Assess for malaria.
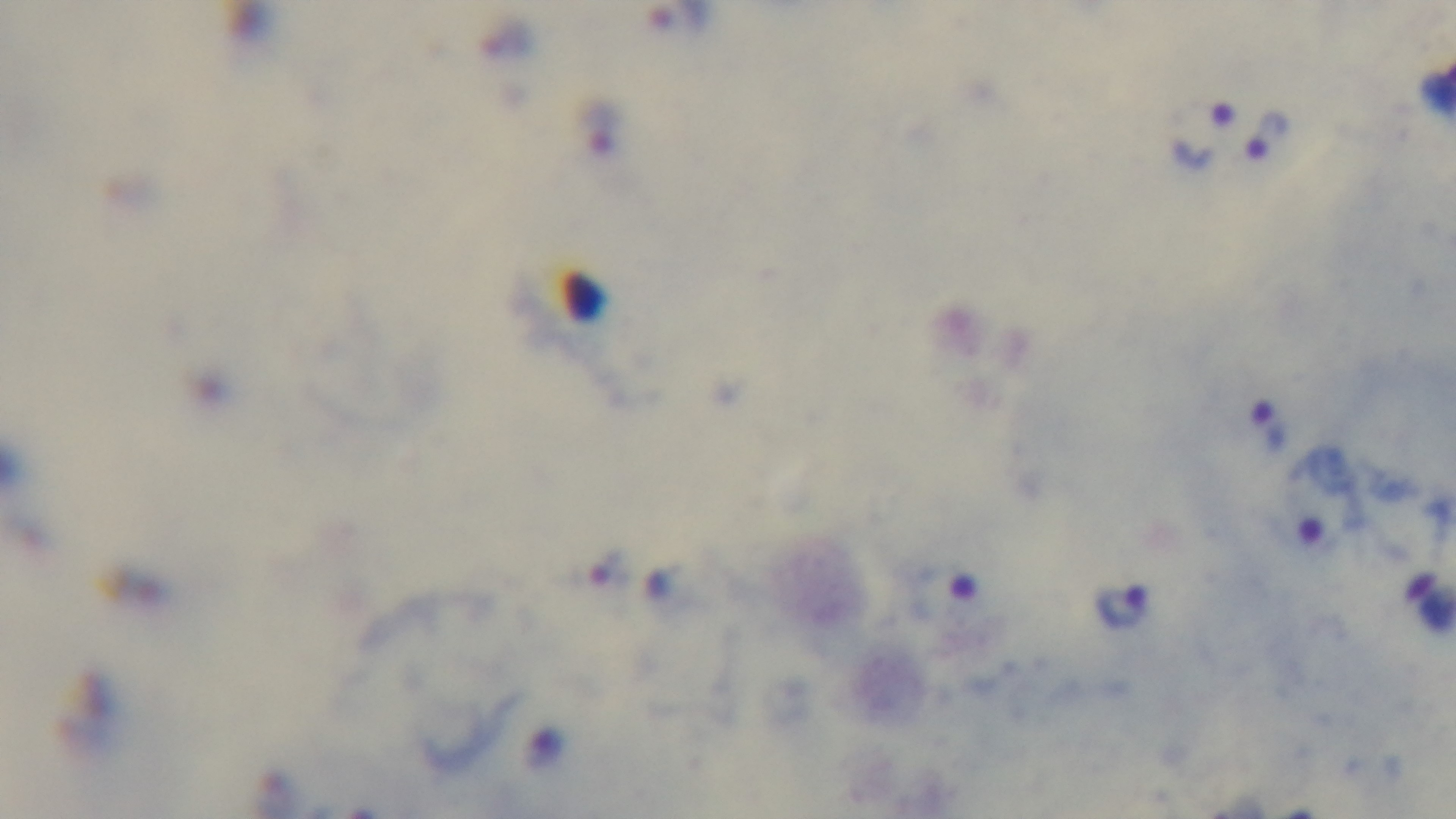
It is infected.

Summary:
  - Field of view: single
  - Preparation: thick
  - Stain: Giemsa
  - Modality: light microscopy
  - Objective: 100x oil immersion
  - Capture: mounted 4K digital camera